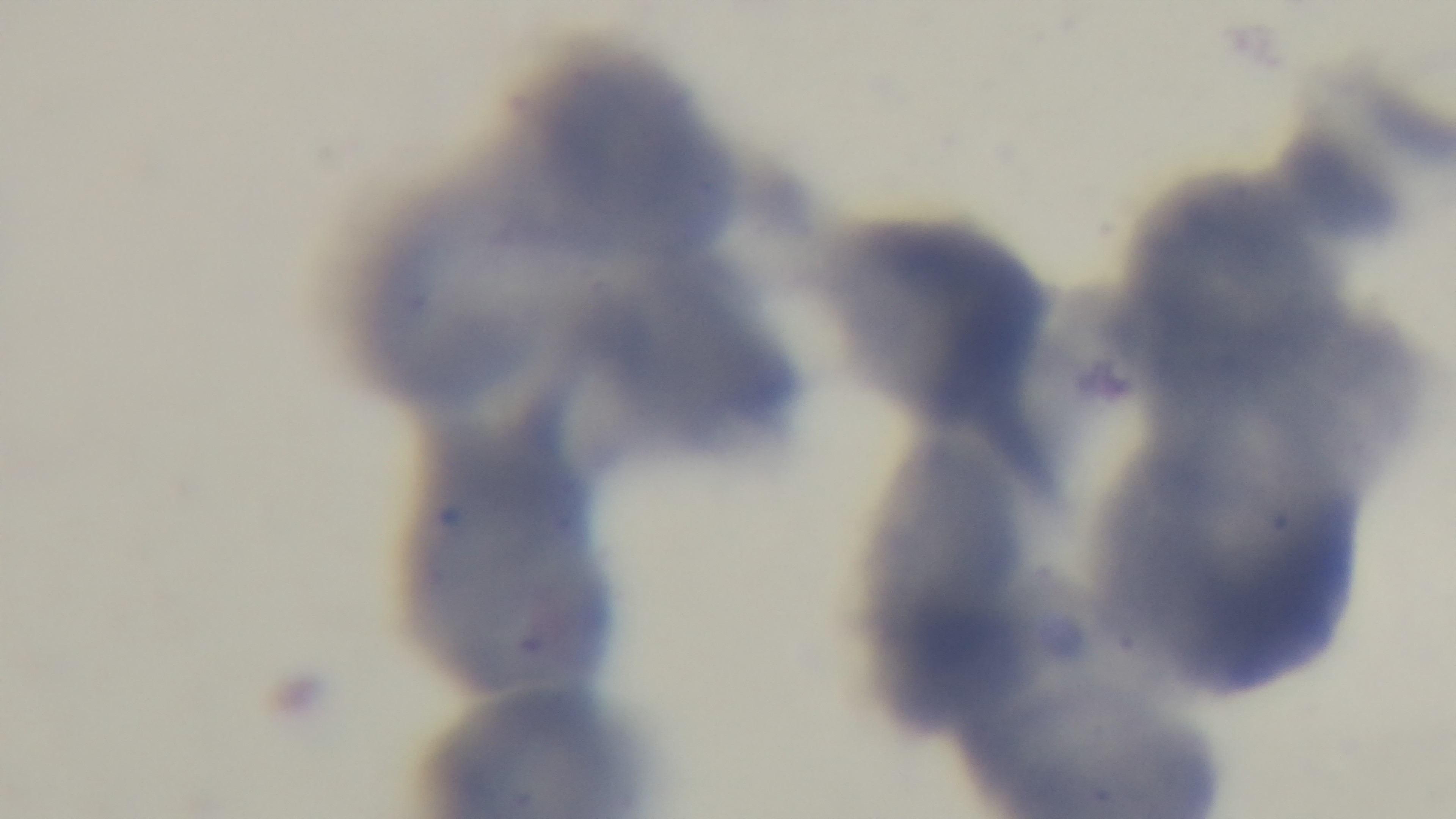
{
  "malaria_status": "negative",
  "modality": "light microscopy",
  "preparation": "thin smear",
  "field_of_view": "single",
  "capture": "mounted 4K digital camera",
  "stain": "Giemsa",
  "objective": "100x oil immersion"
}